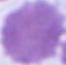
Summary:
  - Identification: red blood cell
  - Modality: micrograph
  - Magnification: 1000x